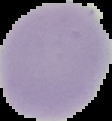

{
  "preparation": "thin blood film",
  "image_size": "112×121 pixels",
  "result": "no malaria parasites seen",
  "image_type": "cell region segmented out of the field of view; surrounding area masked to black"
}